Classify this cell by malaria status.
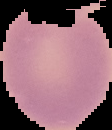
Uninfected.

Image is 112×130 pixels. From a thin blood smear. Cell region segmented out of the field of view; the surrounding area is masked to black.